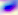
Summary:
  - Identification: Toxoplasma gondii
  - Modality: micrograph
  - Magnification: 400x